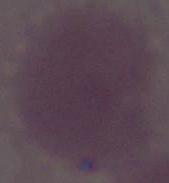

An erythrocyte is seen. 1000x magnification. Photomicrograph.